Point out each Plasmodium parasite.
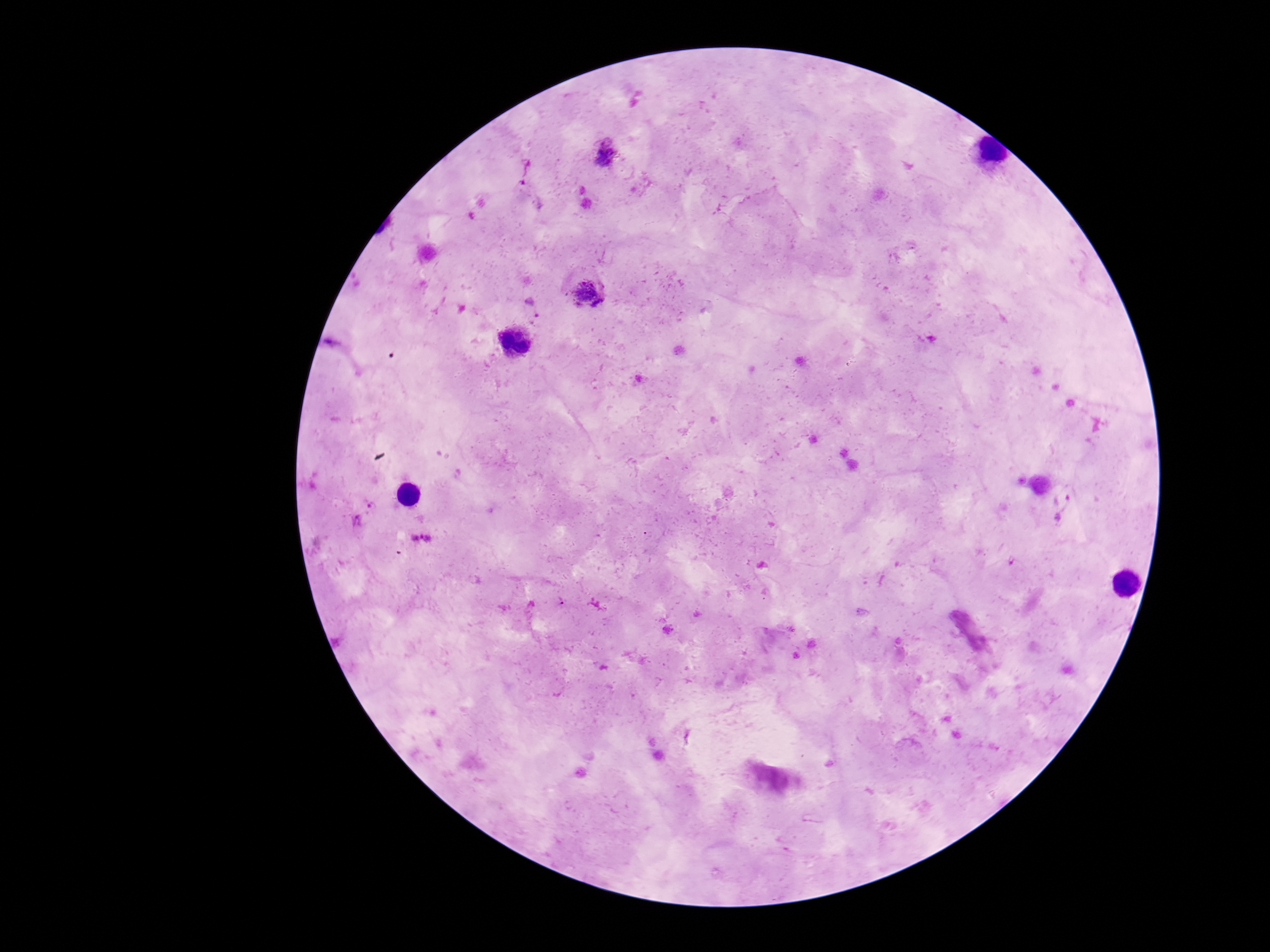

Approximate object centers, in pixels from the top-left corner.
Plasmodium parasites: (x=604, y=154), (x=525, y=171), (x=586, y=294), (x=1064, y=503), (x=420, y=538), (x=561, y=601).

{
  "preparation": "thick blood film",
  "capture": "smartphone camera through the microscope eyepiece",
  "image_size": "1270×952 pixels",
  "magnification": "100x",
  "field_of_view": "single",
  "patient_malaria_status": "positive",
  "stain": "Giemsa"
}